Report the malaria status of this cell.
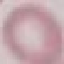

It is uninfected.

stain = Giemsa
image type = automatically extracted cell patch, resized to 64 × 64 pixels
preparation = thin smear
capture = smartphone camera at the microscope eyepiece